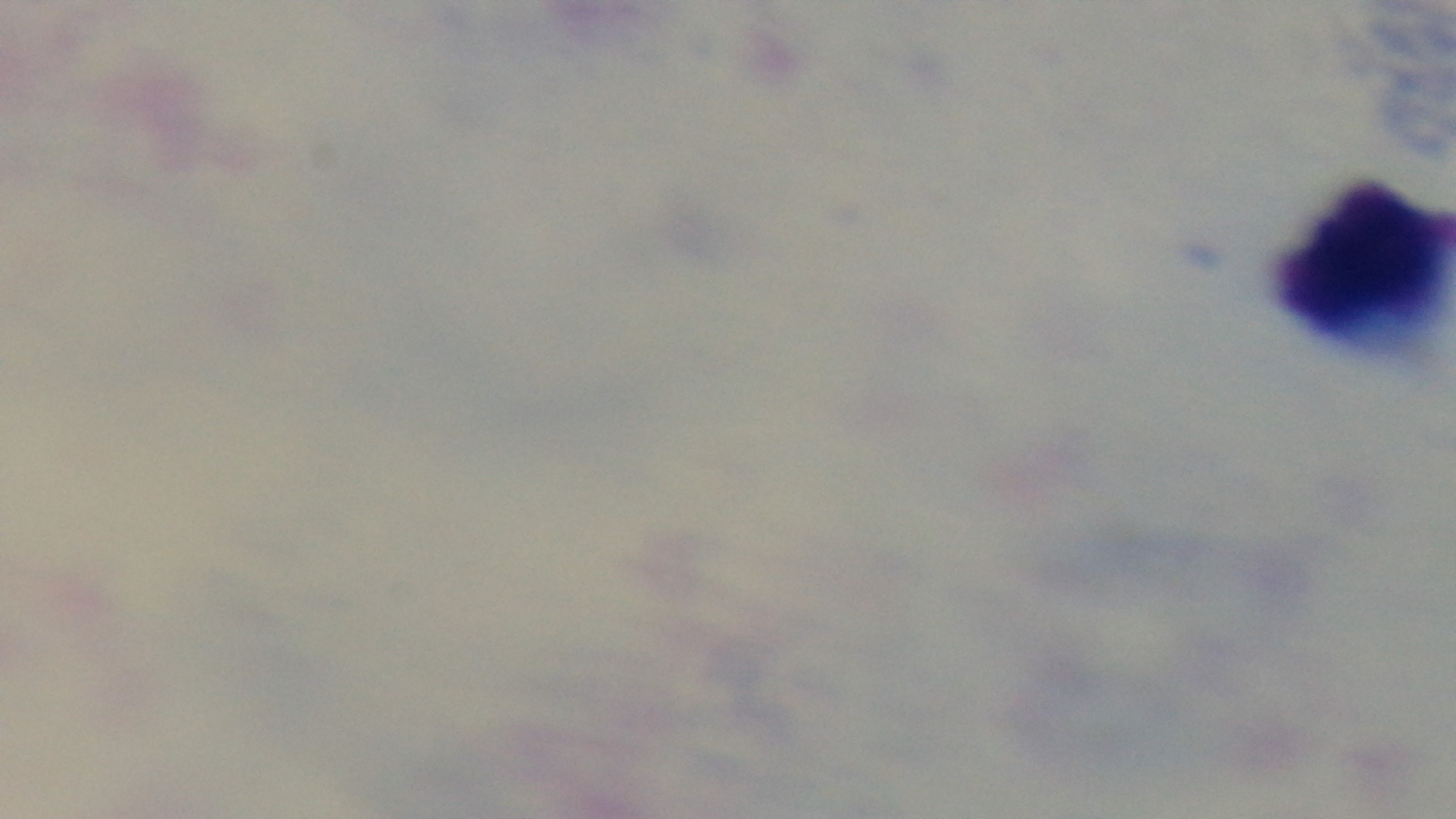

malaria status = uninfected
field of view = single
capture = mounted 4K digital camera
stain = Giemsa
modality = light microscopy
preparation = thick blood film
objective = 100x oil immersion